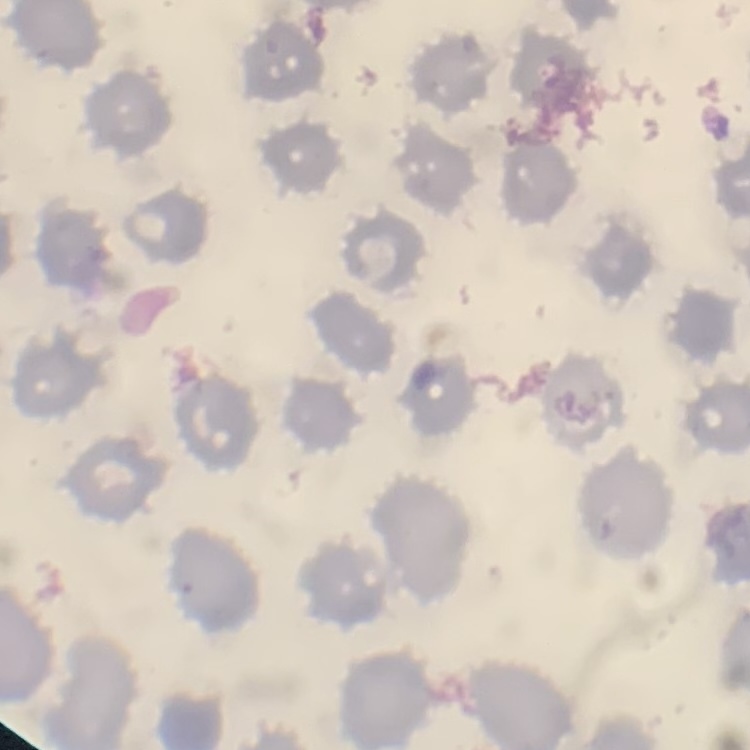
Summary:
  - Red blood cell morphology: no rouleaux formation
  - Image type: one tile cut from a larger photomicrograph
  - Preparation: thin blood smear
  - Stain: Field's or Giemsa